Point out each Plasmodium parasite.
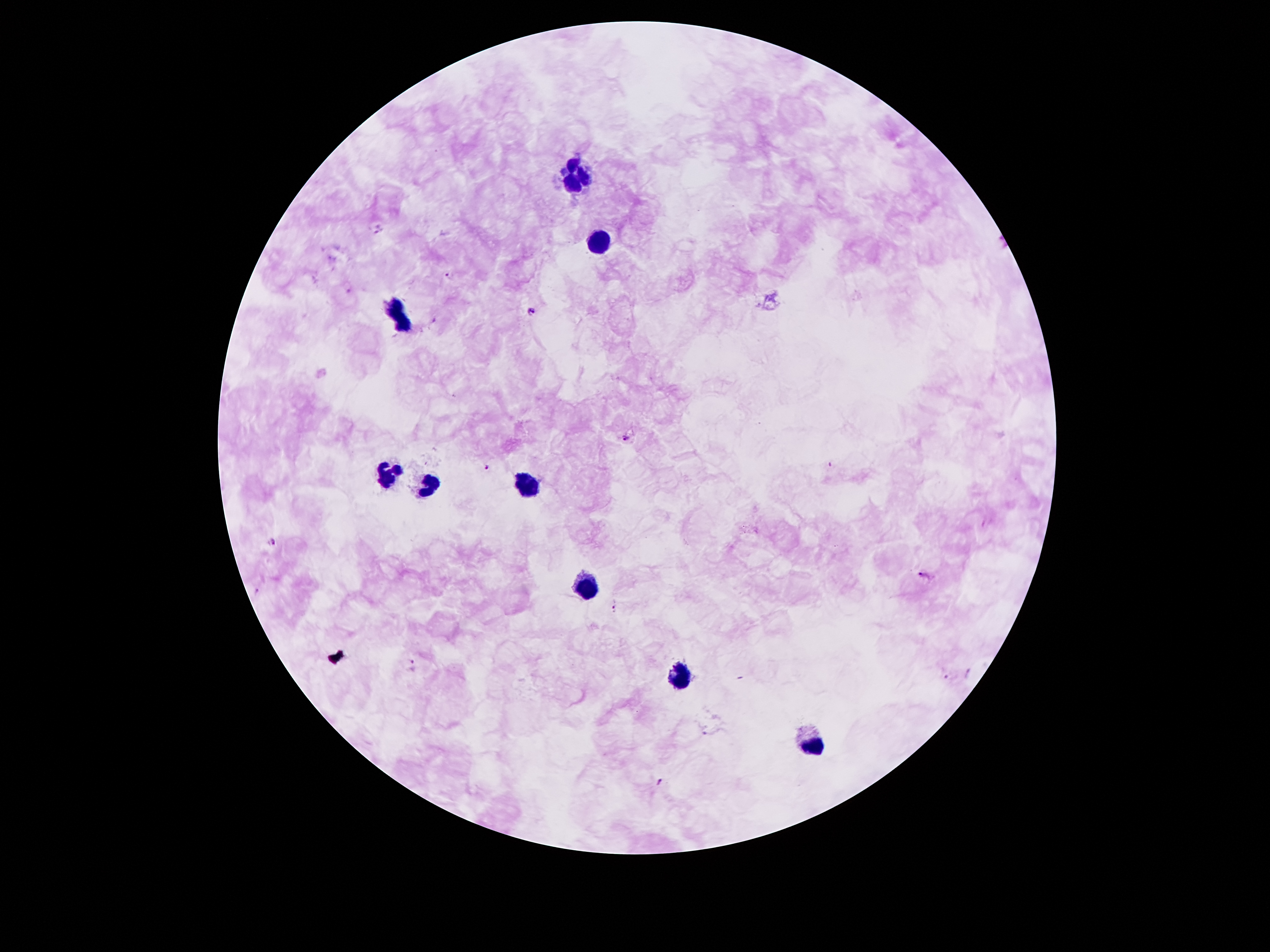
Approximate object centers, in pixels from the top-left corner.
Plasmodium parasites: (x=379, y=231), (x=449, y=275), (x=531, y=311), (x=627, y=440), (x=487, y=467), (x=272, y=541), (x=925, y=576), (x=615, y=605), (x=414, y=663), (x=946, y=678), (x=708, y=735), (x=659, y=782).

Leukocyte locations: (x=574, y=164), (x=585, y=177), (x=571, y=184), (x=602, y=241), (x=396, y=303), (x=403, y=326), (x=388, y=474), (x=430, y=486), (x=522, y=486), (x=583, y=585), (x=676, y=679), (x=808, y=745). One field from this slide. Image is 1270×952 pixels. 100x magnification. Thick blood smear. Photographed through the microscope eyepiece with a smartphone camera. Patient malaria status: positive for Plasmodium falciparum. Giemsa stain.